Report the malaria status of this cell.
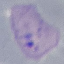
Parasitized.

Summary:
  - Capture: smartphone through the microscope eyepiece
  - Image type: cell patch, automatically extracted from a larger field of view and resized to 64 × 64 pixels
  - Preparation: thin blood film
  - Stain: Giemsa